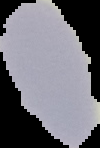
Segmented cell region on a black background. From a thin blood film. Image is 100×148 pixels. Malaria status: uninfected.